Report the malaria status of this cell.
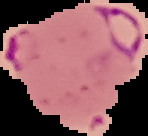

Parasitized.

Image is 148×136 pixels. From a thin blood smear. The area outside the segmented cell region is set to black.